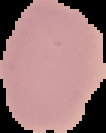
{
  "result": "no Plasmodium parasites seen",
  "preparation": "thin blood film",
  "image_size": "106×133 pixels",
  "image_type": "cell region segmented out of the field of view; surrounding area masked to black"
}